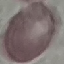
Summary:
  - Malaria status: uninfected
  - Capture: smartphone camera at the microscope eyepiece
  - Image type: automatically extracted cell patch, resized to 64 × 64 pixels
  - Stain: Giemsa
  - Preparation: thin blood film